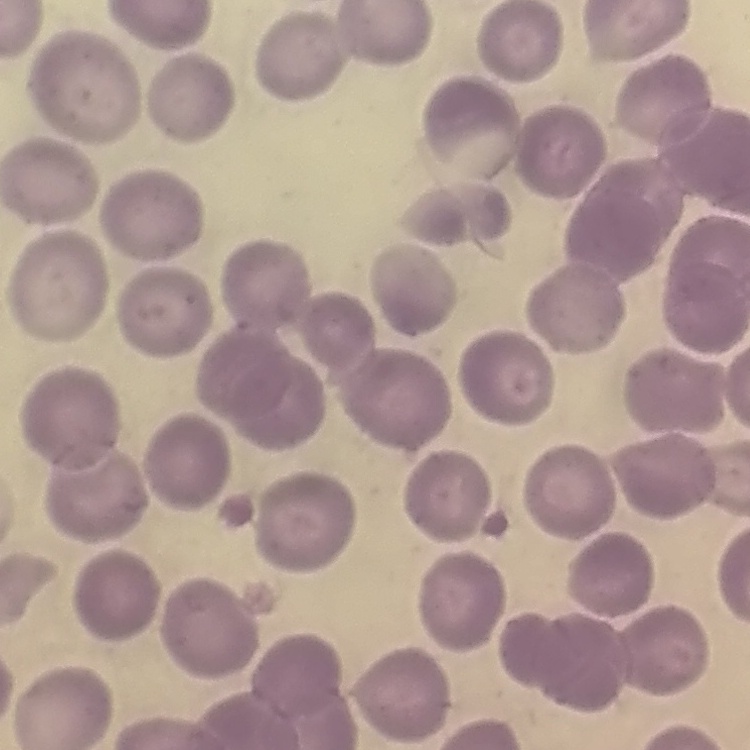

Summary:
  - Red blood cell morphology: no rouleaux formation
  - Preparation: thin peripheral smear
  - Stain: Field's or Giemsa
  - Image type: square crop of a larger photomicrograph